Assess for malaria.
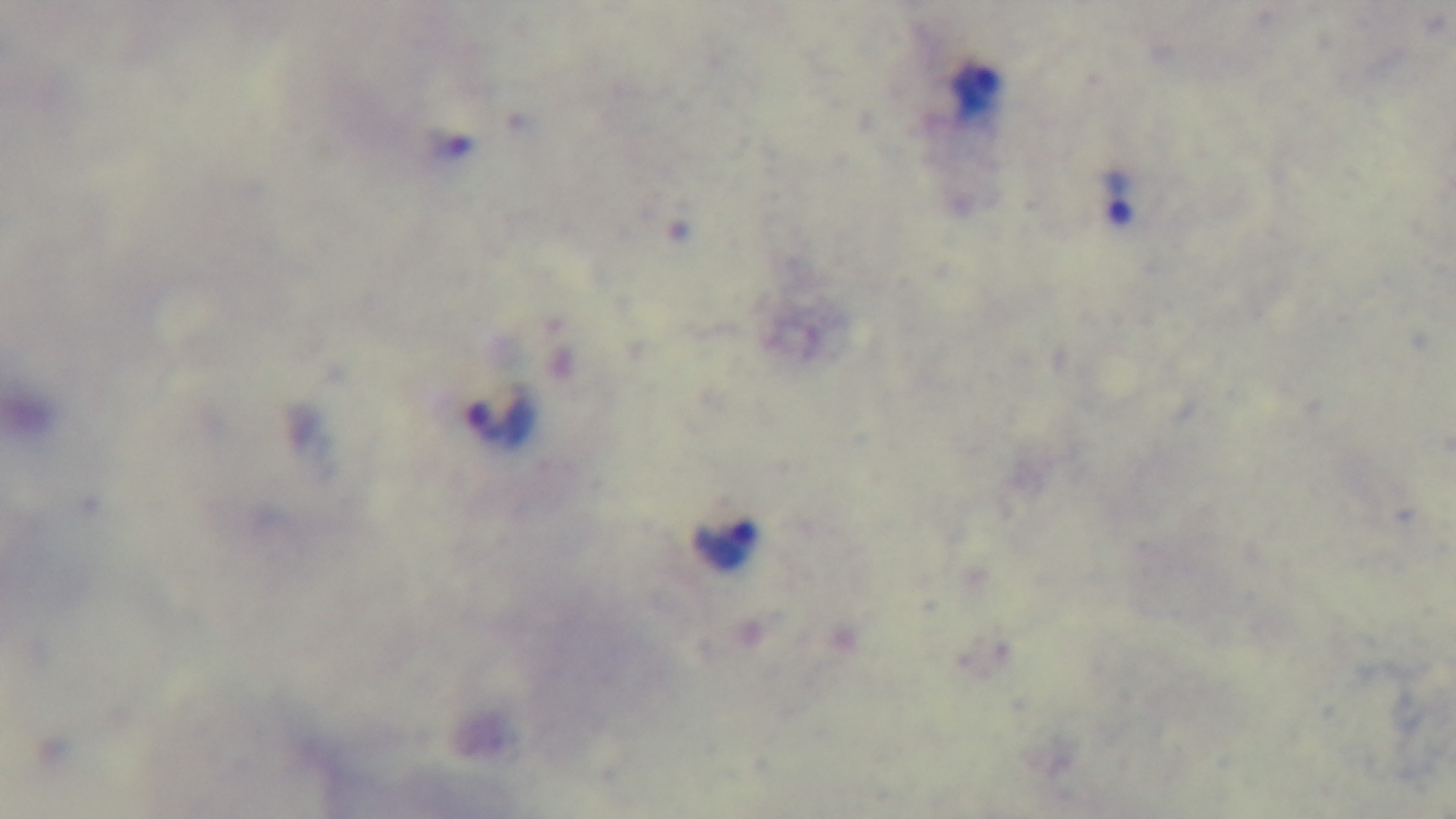

It is infected.

Summary:
  - Capture: mounted 4K digital camera
  - Stain: Giemsa
  - Modality: light microscopy
  - Objective: 100x oil immersion
  - Preparation: thick blood film
  - Field of view: one from the slide